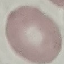
Result: no malaria parasites detected. Automatically extracted cell patch, resized to 64 × 64 pixels. Thin blood smear. Giemsa stain. Acquired by smartphone through the microscope eyepiece.